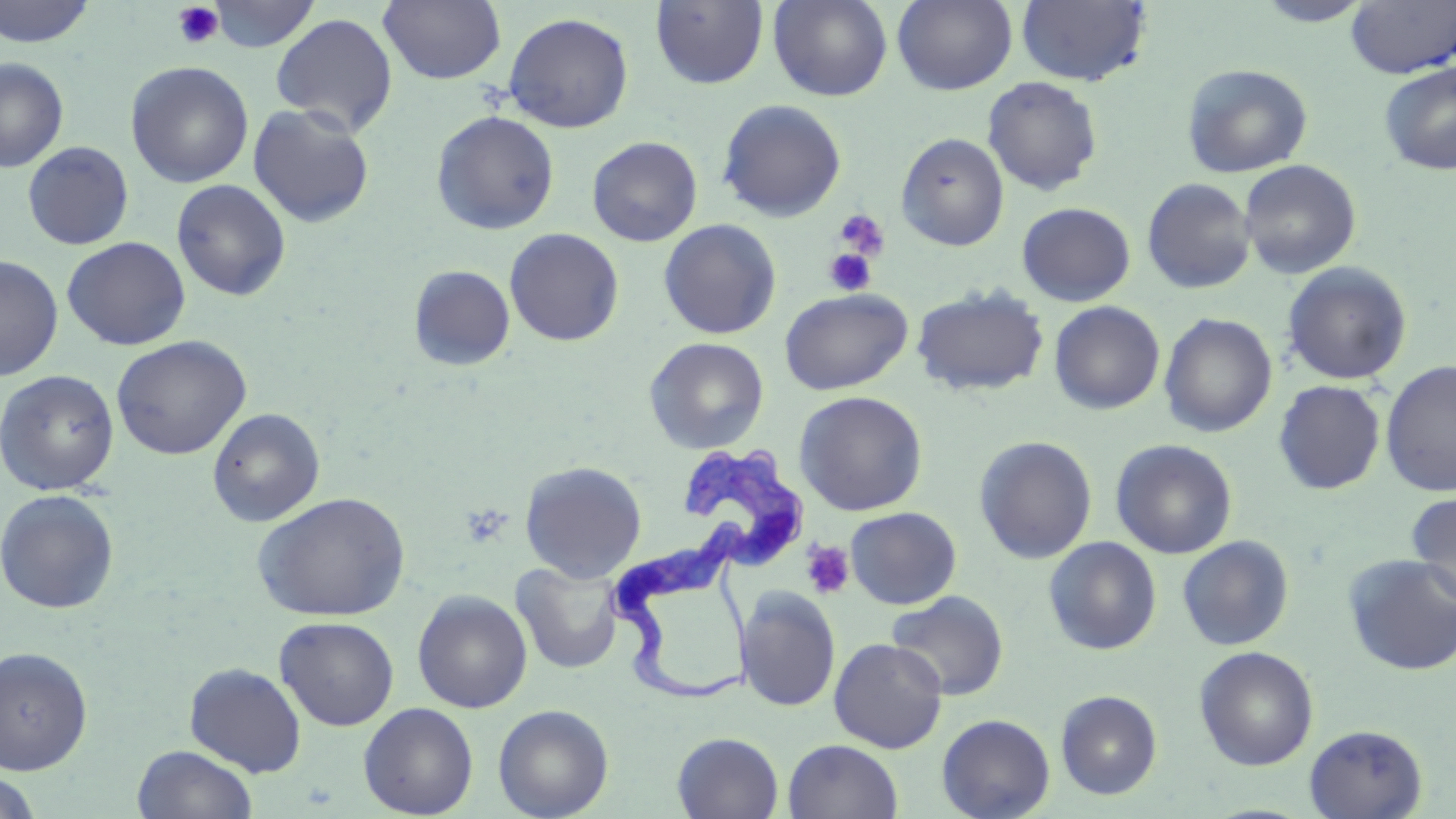

slide-level diagnosis = Trypanosoma brucei
field of view = single
stain = May-Grünwald-Giemsa
modality = optical microscopy
preparation = thin blood smear
image size = 1456×819 pixels
magnification = 1000x
uninfected red blood cell locations = approximate bounding boxes as (x1,y1)-(x2,y2) corner pairs in pixels: (0,0)-(96,47), (208,0)-(319,52), (768,0)-(892,102), (892,0)-(1017,94), (1250,0)-(1376,26), (379,1)-(507,85), (650,1)-(769,90), (1016,1)-(1152,87), (1347,1)-(1456,79), (503,12)-(634,133), (270,13)-(398,136), (0,58)-(68,172), (125,61)-(254,187), (1379,62)-(1456,176), (1181,63)-(1313,178), (982,76)-(1103,196), (717,99)-(847,222), (247,103)-(375,228), (431,110)-(559,235), (896,132)-(1009,251), (587,136)-(702,247), (22,141)-(134,250), (1239,159)-(1361,279), (1141,177)-(1256,294), (171,179)-(291,301), (1017,202)-(1136,306), (659,219)-(782,339), (504,228)-(624,346), (62,236)-(191,350), (0,255)-(63,381), (1281,261)-(1412,385), (409,265)-(516,371), (911,285)-(1049,398), (780,288)-(912,395), (1049,301)-(1165,415), (1159,312)-(1277,437), (111,335)-(252,460), (644,336)-(769,454), (1380,360)-(1456,496), (0,369)-(120,495), (1273,380)-(1387,495), (793,391)-(928,516), (207,407)-(325,527), (974,435)-(1098,564), (1110,439)-(1237,559), (519,460)-(647,582), (0,488)-(119,614), (1406,490)-(1456,605), (253,492)-(410,621), (846,507)-(961,609), (1177,535)-(1294,651), (1043,536)-(1162,655), (1343,553)-(1456,676), (511,561)-(624,674), (736,586)-(841,712), (412,589)-(532,713), (886,590)-(1009,701), (274,616)-(399,731), (828,637)-(948,753), (0,646)-(93,775), (1194,646)-(1318,771), (184,662)-(307,776), (1055,690)-(1162,799), (358,702)-(478,818), (493,704)-(614,819), (937,713)-(1055,819), (1304,724)-(1428,818), (672,732)-(784,819), (782,739)-(903,819), (131,744)-(259,819), (0,771)-(42,819)
Trypanosoma brucei locations = approximate bounding boxes as (x1,y1)-(x2,y2) corner pairs in pixels: (608,446)-(810,706)
platelet locations = approximate bounding boxes as (x1,y1)-(x2,y2) corner pairs in pixels: (172,2)-(225,49), (834,207)-(890,262), (824,248)-(876,296), (800,540)-(855,599)